Report the malaria status of this cell.
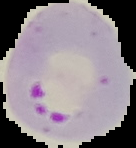

It is parasitized.

Summary:
  - Image size: 136×148 pixels
  - Preparation: thin blood smear
  - Image type: segmented cell region with the area outside set to black